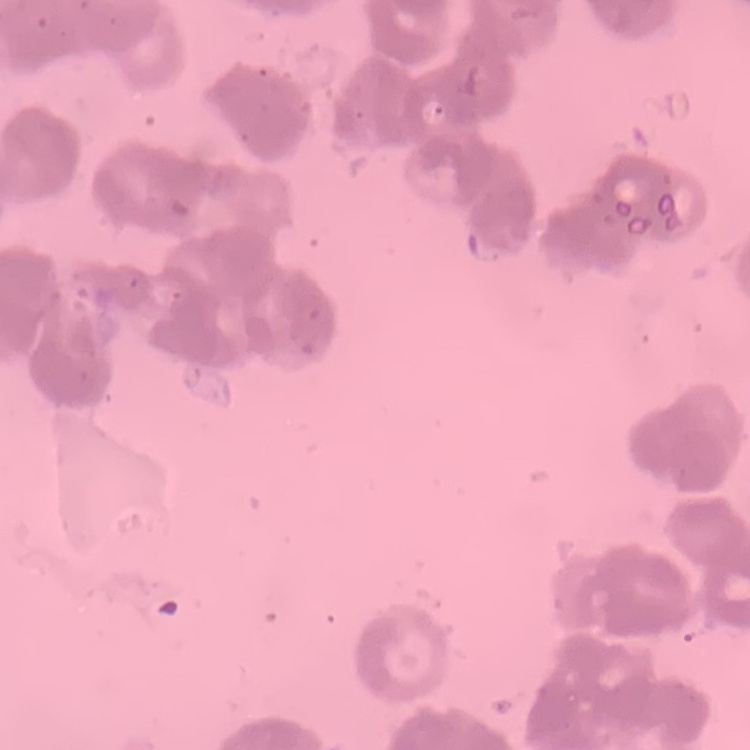
The red blood cells exhibit rouleaux formation. Field's or Giemsa stain. Thin peripheral smear. One tile cut from a larger photomicrograph.